Assess this cell for malaria.
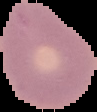
Uninfected.

Segmented cell region on a black background. From a thin blood film. Image is 97×112 pixels.